Report the malaria status of this cell.
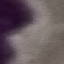

It is uninfected.

Summary:
  - Stain: Giemsa
  - Image type: automatically extracted cell patch, resized to 64 × 64 pixels
  - Capture: smartphone through the microscope eyepiece
  - Preparation: thin blood film